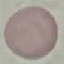

Result: no malaria parasites seen. Thin blood smear. Photographed with a smartphone camera at the microscope eyepiece. Automatically extracted cell patch, resized to 64 × 64 pixels. Giemsa stain.